Assess the morphology of the red blood cells.
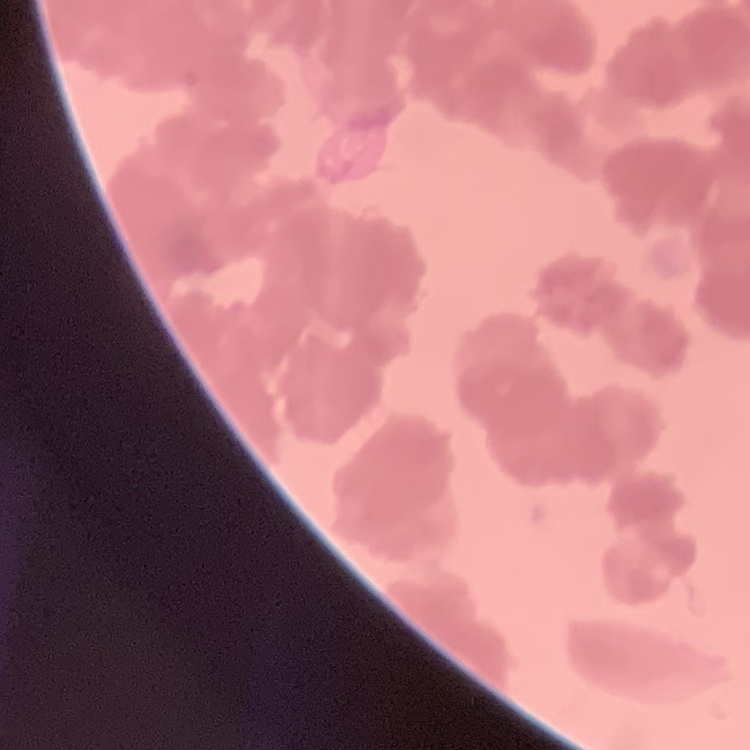

Rouleaux formation.

Summary:
  - Stain: Field's or Giemsa
  - Preparation: thin blood smear
  - Image type: one tile cut from a larger photomicrograph